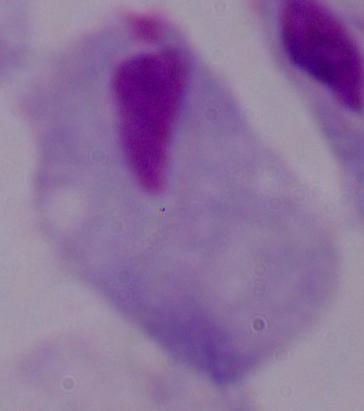

Summary:
  - Modality: photomicrograph
  - Identification: trichomonad
  - Magnification: 1000x